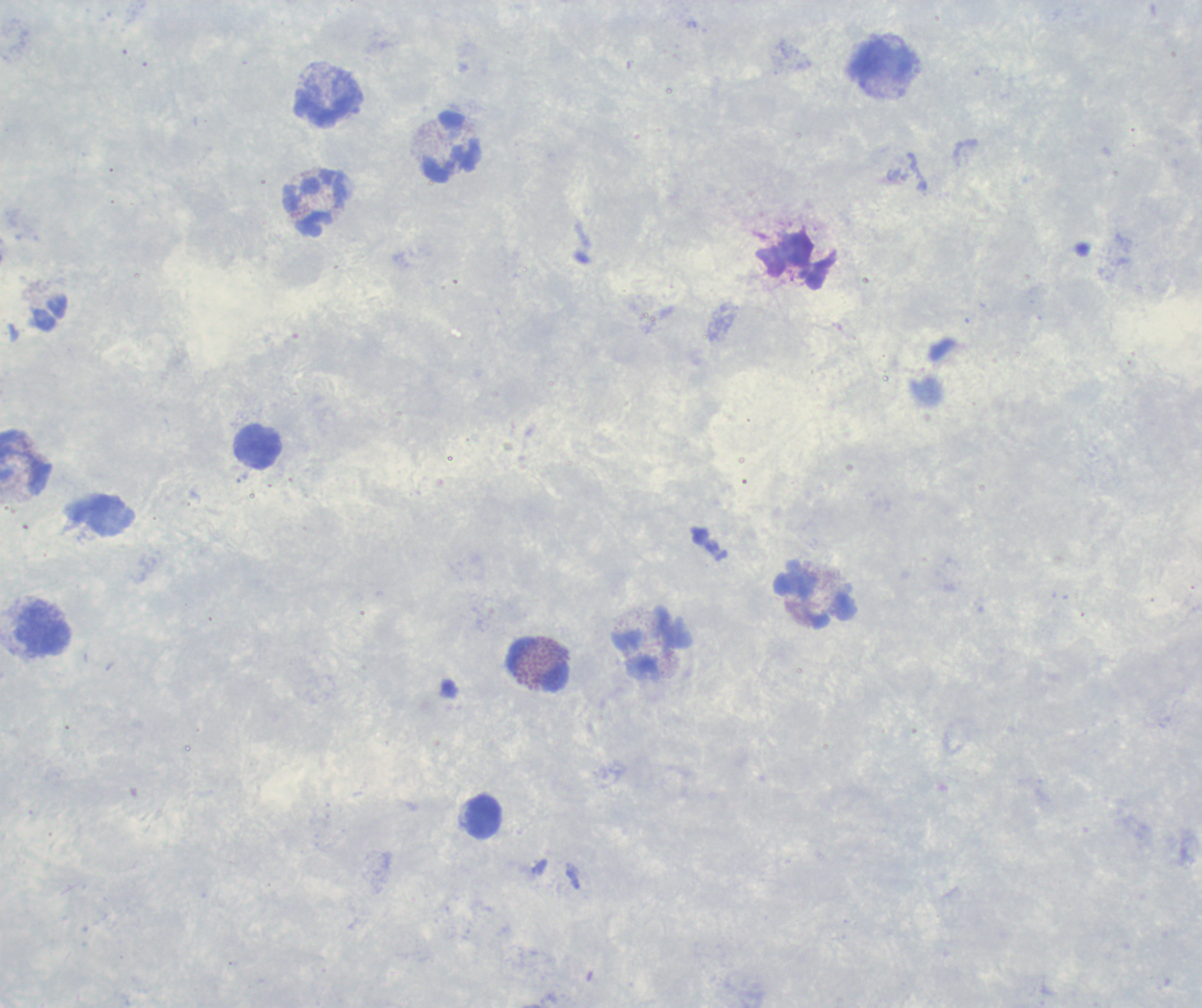

Approximate centers as {x, y} in pixels. Leukocyte locations: {885, 62}, {327, 102}, {452, 146}, {314, 204}, {795, 261}, {258, 448}, {25, 462}, {816, 599}, {43, 631}, {537, 665}, {484, 818}. Previously used in a real diagnosis. Coloration quality: good. Background quality: poor. Image is 1202×1008 pixels. 100x magnification. One field from this slide. Result: negative for Plasmodium parasites. Thick smear of blood. Romanowsky-stained preparation.